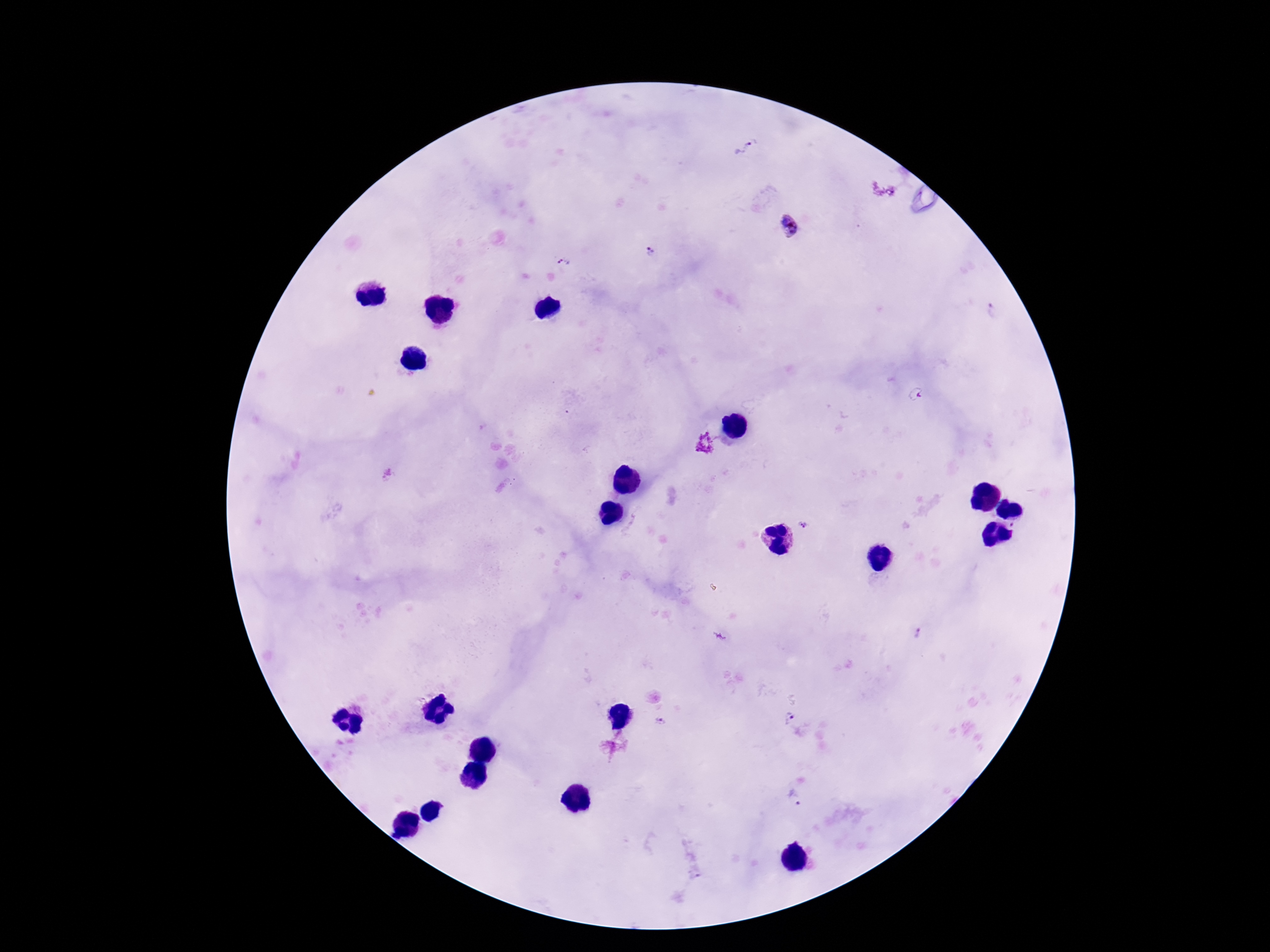 Approximate centers as (x, y) in pixels. Plasmodium parasite locations: (745, 147), (790, 226), (649, 252), (564, 262), (993, 312), (704, 443), (803, 524), (917, 633), (788, 716), (660, 721), (795, 797). Thick peripheral-blood smear. Patient malaria status: infected. 100x magnification. Image is 1270×952 pixels. Photographed through the microscope eyepiece with a smartphone camera. One field from this slide. Giemsa-stained preparation.